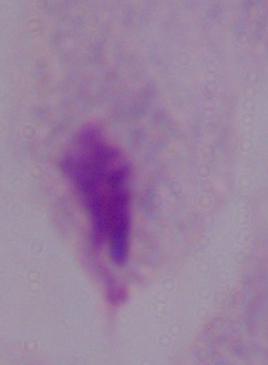
magnification = 1000x
identification = trichomonad
modality = micrograph